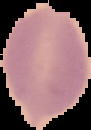
preparation = thin blood film
image size = 91×130 pixels
malaria status = uninfected
image type = segmented cell region on a black background